Draw a bounding box around every malaria parasite.
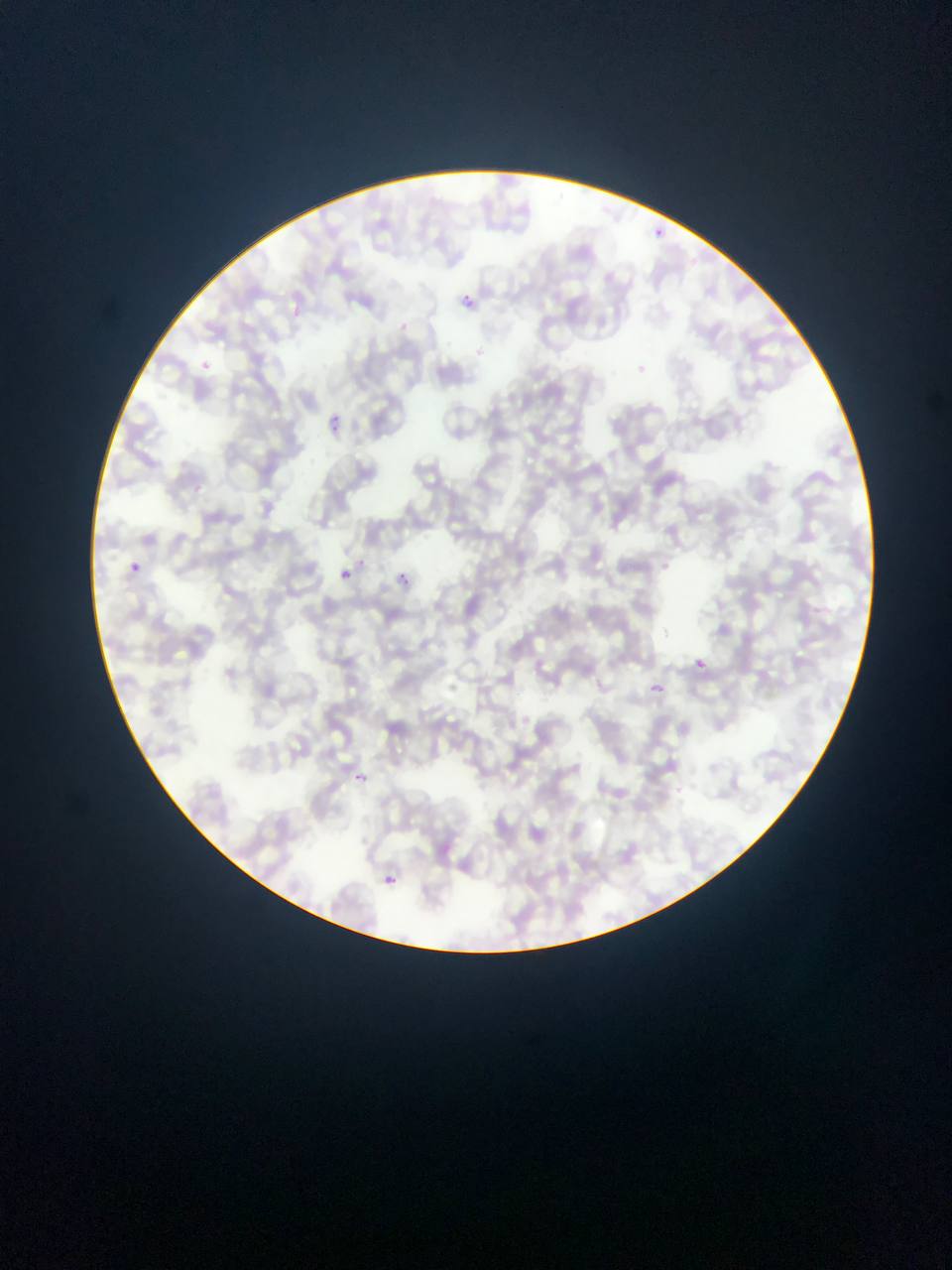

Approximate bounding boxes as (left, top, right, bottom) in pixels.
Malaria parasites: (323, 411, 345, 433), (130, 561, 142, 573), (339, 564, 361, 585), (393, 567, 421, 585), (690, 656, 711, 675), (648, 677, 676, 698), (356, 773, 365, 781), (382, 872, 402, 885).

Photographed through a microscope with a mobile-phone camera. Image is 952×1270 pixels. One field of view. Thin blood smear. Sample from Ghana.